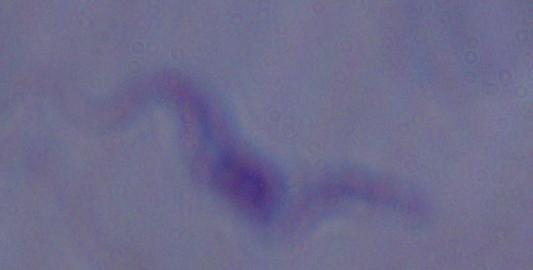
Summary:
  - Magnification: 1000x
  - Identification: trypanosome
  - Modality: micrograph